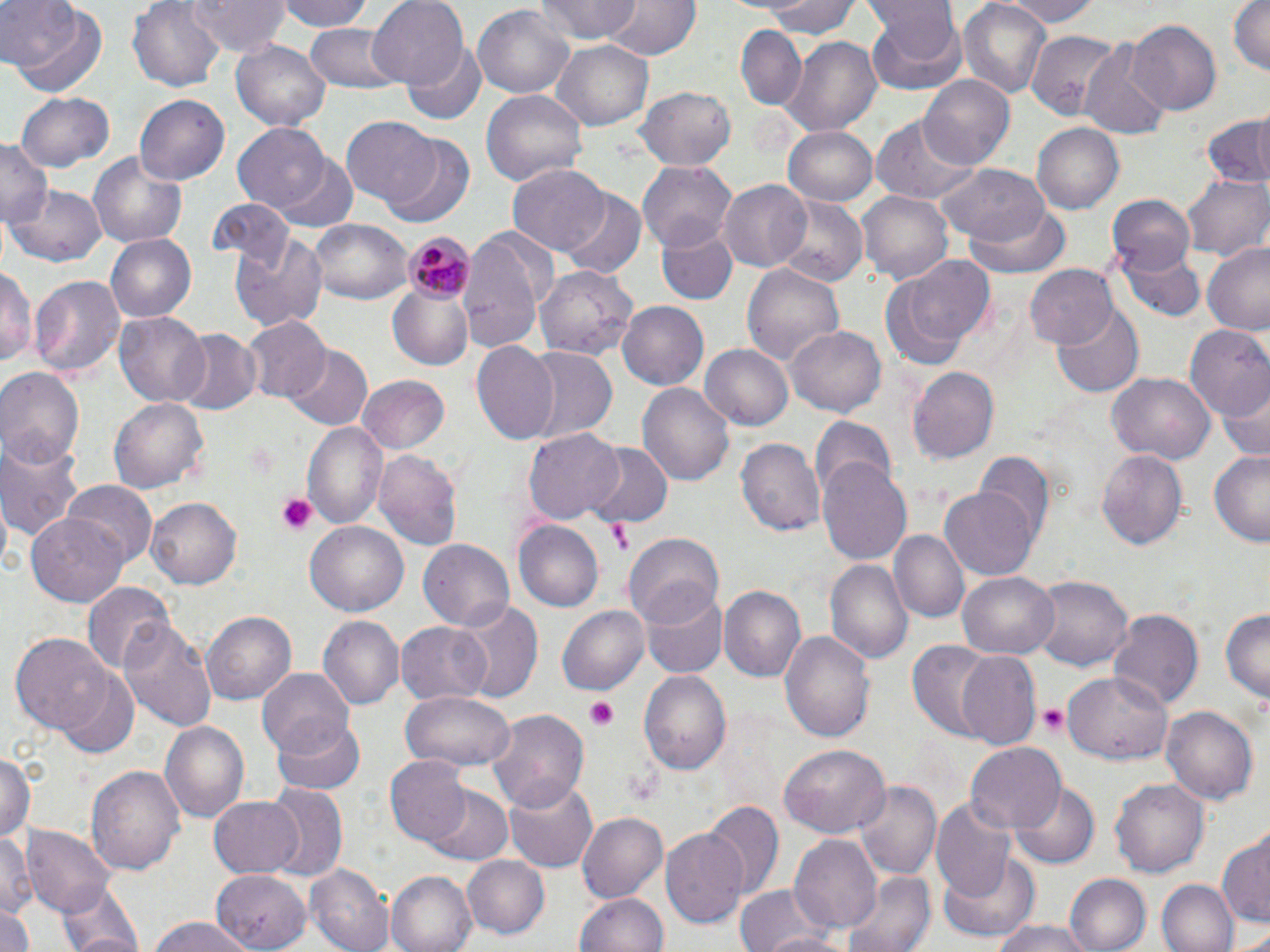
{
  "slide_level_diagnosis": "Plasmodium malariae",
  "uninfected_red_blood_cell_locations": "approximate bounding boxes as [x1, y1, x2, y2] in pixels: [1, 0, 104, 94], [190, 0, 290, 54], [276, 0, 378, 30], [368, 0, 468, 90], [536, 0, 641, 45], [607, 0, 699, 61], [762, 0, 863, 40], [959, 0, 1052, 97], [995, 0, 1102, 26], [1228, 0, 1269, 79], [128, 1, 225, 90], [862, 3, 965, 95], [474, 4, 576, 100], [1124, 18, 1222, 116], [305, 21, 403, 92], [736, 26, 807, 112], [1026, 31, 1129, 121], [781, 35, 882, 135], [232, 37, 331, 130], [550, 39, 657, 132], [405, 44, 486, 123], [1081, 44, 1171, 138], [920, 75, 1015, 170], [636, 86, 738, 169], [481, 90, 588, 190], [18, 92, 113, 174], [134, 95, 229, 187], [871, 115, 980, 207], [1200, 115, 1270, 187], [341, 118, 442, 206], [1032, 123, 1124, 214], [233, 124, 332, 212], [783, 126, 879, 207], [381, 136, 473, 227], [0, 140, 51, 230], [89, 150, 189, 249], [272, 154, 359, 232], [638, 161, 736, 247], [506, 163, 611, 256], [935, 164, 1050, 250], [1181, 173, 1269, 261], [717, 179, 814, 273], [8, 183, 107, 269], [560, 188, 648, 278], [857, 193, 953, 282], [1106, 193, 1197, 272], [769, 198, 867, 287], [209, 199, 294, 271], [962, 200, 1072, 280], [308, 217, 413, 306], [656, 224, 738, 306], [457, 229, 554, 352], [230, 232, 328, 331], [105, 234, 196, 322], [1202, 244, 1270, 335], [1119, 247, 1204, 323], [895, 253, 996, 355], [741, 261, 844, 369], [536, 262, 641, 360], [1025, 263, 1119, 349], [0, 265, 36, 369], [30, 273, 126, 379], [390, 287, 472, 368], [616, 301, 707, 392], [1052, 306, 1143, 396], [117, 313, 210, 407], [244, 317, 332, 403], [1184, 322, 1270, 422], [787, 324, 886, 418], [171, 330, 262, 416], [472, 341, 561, 445], [701, 343, 795, 431], [283, 346, 372, 430], [522, 346, 618, 443], [0, 366, 85, 466], [907, 366, 1003, 465], [1109, 372, 1214, 464], [359, 376, 450, 454], [1221, 378, 1270, 465], [638, 382, 734, 486], [108, 397, 209, 494], [809, 418, 897, 500], [302, 421, 387, 530], [525, 429, 625, 522], [0, 434, 87, 545], [736, 438, 825, 537], [583, 443, 672, 529], [373, 447, 465, 555], [1097, 449, 1190, 551], [1208, 452, 1270, 545], [975, 453, 1054, 547], [817, 457, 912, 566], [63, 482, 158, 566], [939, 485, 1038, 582], [147, 497, 243, 590], [29, 512, 131, 606], [305, 520, 408, 618], [515, 520, 603, 609], [890, 530, 969, 625], [625, 532, 725, 628], [419, 540, 512, 632], [826, 559, 913, 667], [958, 571, 1057, 658], [1030, 575, 1135, 672], [84, 582, 174, 674], [719, 585, 808, 682], [642, 591, 727, 678], [452, 598, 544, 704], [559, 606, 648, 693], [1219, 607, 1270, 707], [1107, 608, 1204, 712], [201, 610, 296, 706], [119, 615, 219, 733], [318, 616, 401, 711], [395, 620, 492, 706], [779, 630, 876, 743], [11, 633, 113, 734], [905, 640, 1004, 742], [955, 650, 1039, 749], [256, 667, 355, 757], [59, 669, 139, 757], [640, 669, 731, 778], [1062, 671, 1174, 764], [401, 691, 515, 771], [1164, 706, 1258, 806], [485, 707, 591, 814], [270, 716, 366, 794], [160, 720, 250, 823], [962, 742, 1067, 835], [778, 744, 890, 839], [0, 752, 35, 845], [386, 754, 472, 847], [87, 764, 186, 879], [505, 778, 597, 871], [1110, 778, 1209, 877], [854, 780, 941, 881], [1012, 780, 1099, 866], [425, 785, 512, 866], [265, 786, 348, 883], [206, 794, 305, 878], [932, 799, 1017, 905], [701, 802, 783, 900], [577, 811, 669, 903], [25, 826, 115, 916], [0, 830, 36, 917], [660, 830, 748, 930], [789, 836, 882, 935], [1216, 836, 1269, 928], [938, 852, 1040, 943], [463, 855, 551, 938], [307, 863, 393, 952], [210, 868, 311, 948], [841, 869, 939, 952], [389, 870, 477, 952], [1066, 874, 1151, 952], [1157, 878, 1238, 952], [55, 880, 148, 952], [731, 883, 838, 952], [577, 891, 668, 951], [1, 907, 36, 952], [752, 913, 850, 952], [144, 917, 258, 952], [987, 919, 1098, 952], [1236, 928, 1270, 952]",
  "platelet_locations": "approximate bounding boxes as [x1, y1, x2, y2] in pixels: [274, 494, 320, 536], [606, 518, 633, 554], [586, 700, 618, 731], [1036, 703, 1071, 737], [627, 769, 663, 807]",
  "image_size": "1270×952 pixels",
  "field_of_view": "one of a larger specimen",
  "modality": "optical microscopy",
  "stain": "May-Grünwald-Giemsa",
  "plasmodium_malariae_infected_red_blood_cell_locations": "approximate bounding boxes as [x1, y1, x2, y2] in pixels: [405, 234, 475, 305]",
  "magnification": "1000x",
  "preparation": "thin blood film"
}